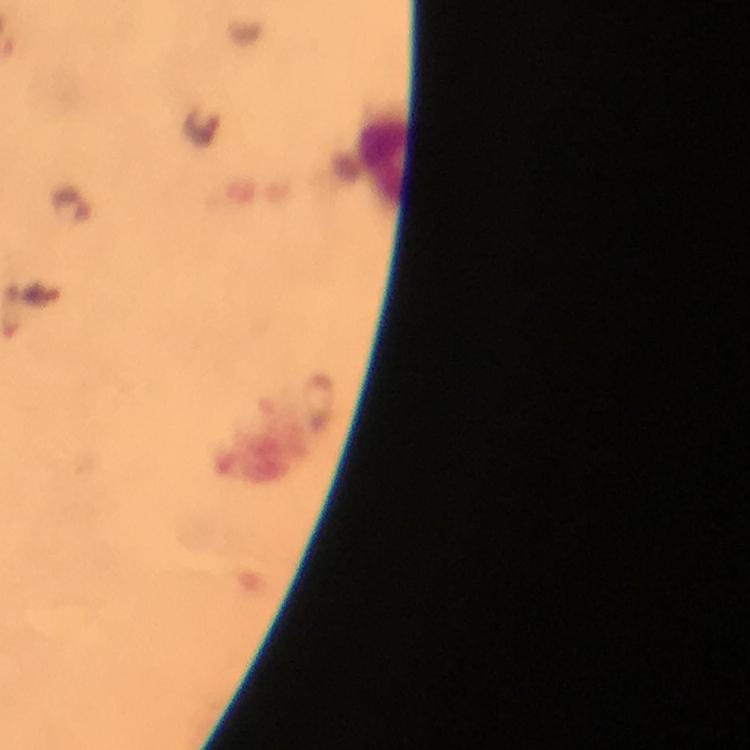
capture = smartphone camera through the microscope
cropped from = one field of view
image size = 750×750 pixels
stain = Giemsa
Plasmodium parasite locations = approximate object centers, in pixels from the top-left corner: (x=71, y=204)
immersion oil = used
preparation = thick blood smear
magnification = 100x
leukocyte locations = approximate object centers, in pixels from the top-left corner: (x=385, y=160)
context = from a diagnostic examination for malaria